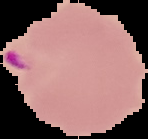

Summary:
  - Image type: segmented cell region on a black background
  - Image size: 148×139 pixels
  - Malaria status: parasitized
  - Preparation: thin blood smear